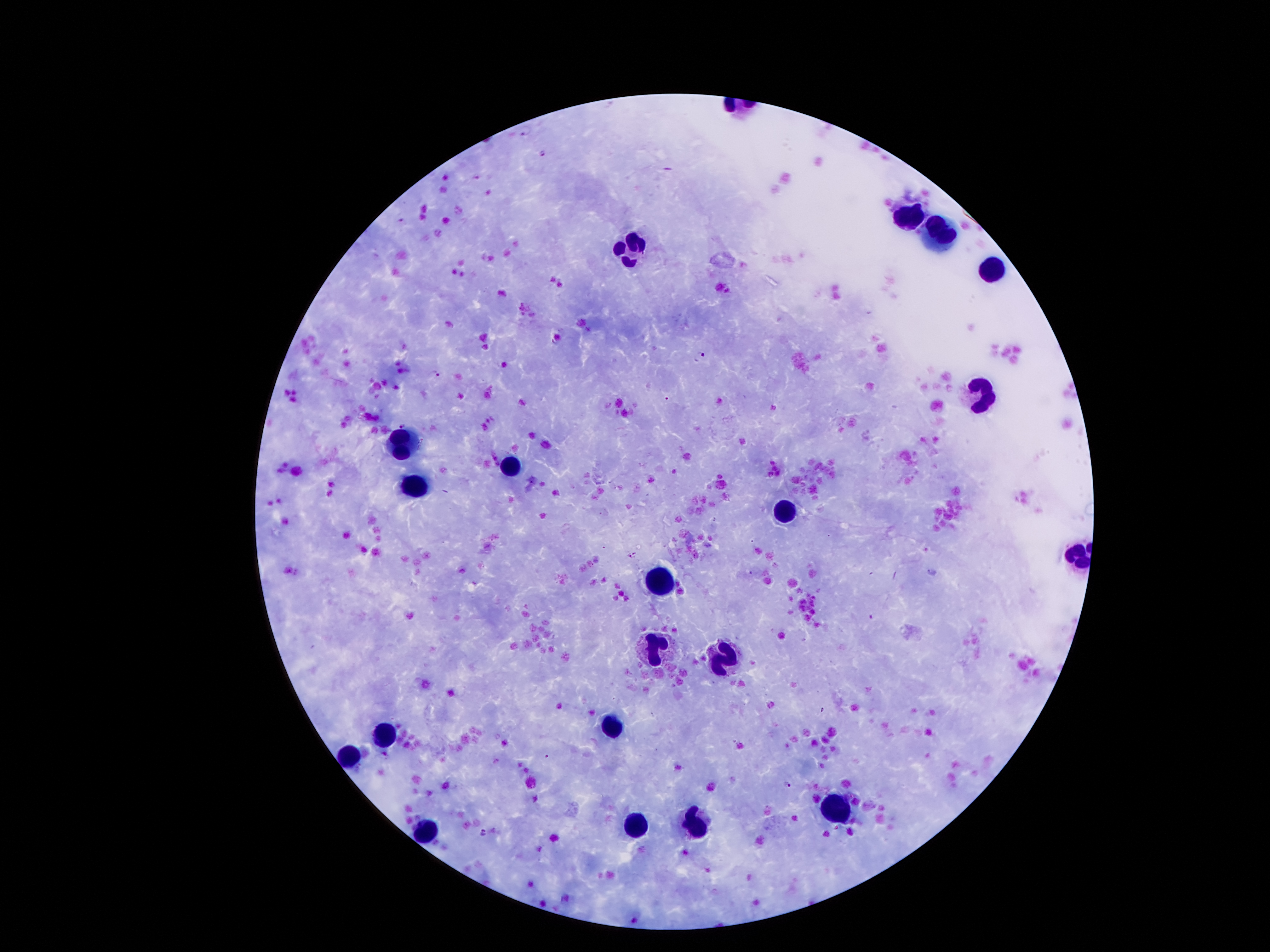
Approximate centers as {x, y} in pixels.
Summary:
  - Leukocyte locations: {908, 219}, {929, 232}, {631, 249}, {992, 267}, {983, 396}, {402, 444}, {511, 471}, {416, 491}, {786, 510}, {658, 580}, {654, 644}, {729, 657}, {611, 726}, {384, 735}, {350, 758}, {835, 810}, {699, 824}, {636, 826}, {429, 834}
  - Malaria parasite locations: {527, 129}, {543, 152}, {701, 355}, {436, 375}, {667, 397}, {404, 425}, {753, 541}, {926, 550}, {634, 555}, {873, 616}, {547, 757}, {788, 785}, {484, 832}
  - Preparation: thick blood film
  - Stain: Giemsa
  - Magnification: 100x
  - Field of view: single
  - Capture: smartphone camera through the microscope eyepiece
  - Patient malaria status: positive for Plasmodium falciparum
  - Image size: 1270×952 pixels